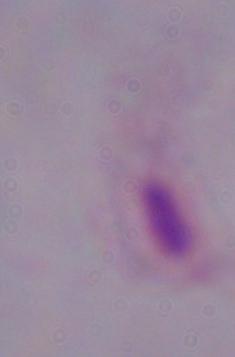 Captured at 1000x magnification. Micrograph. A trichomonad is shown.